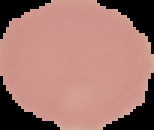

Result: no Plasmodium parasites detected. Image is 154×130 pixels. From a thin blood smear. Segmented cell region on a black background.